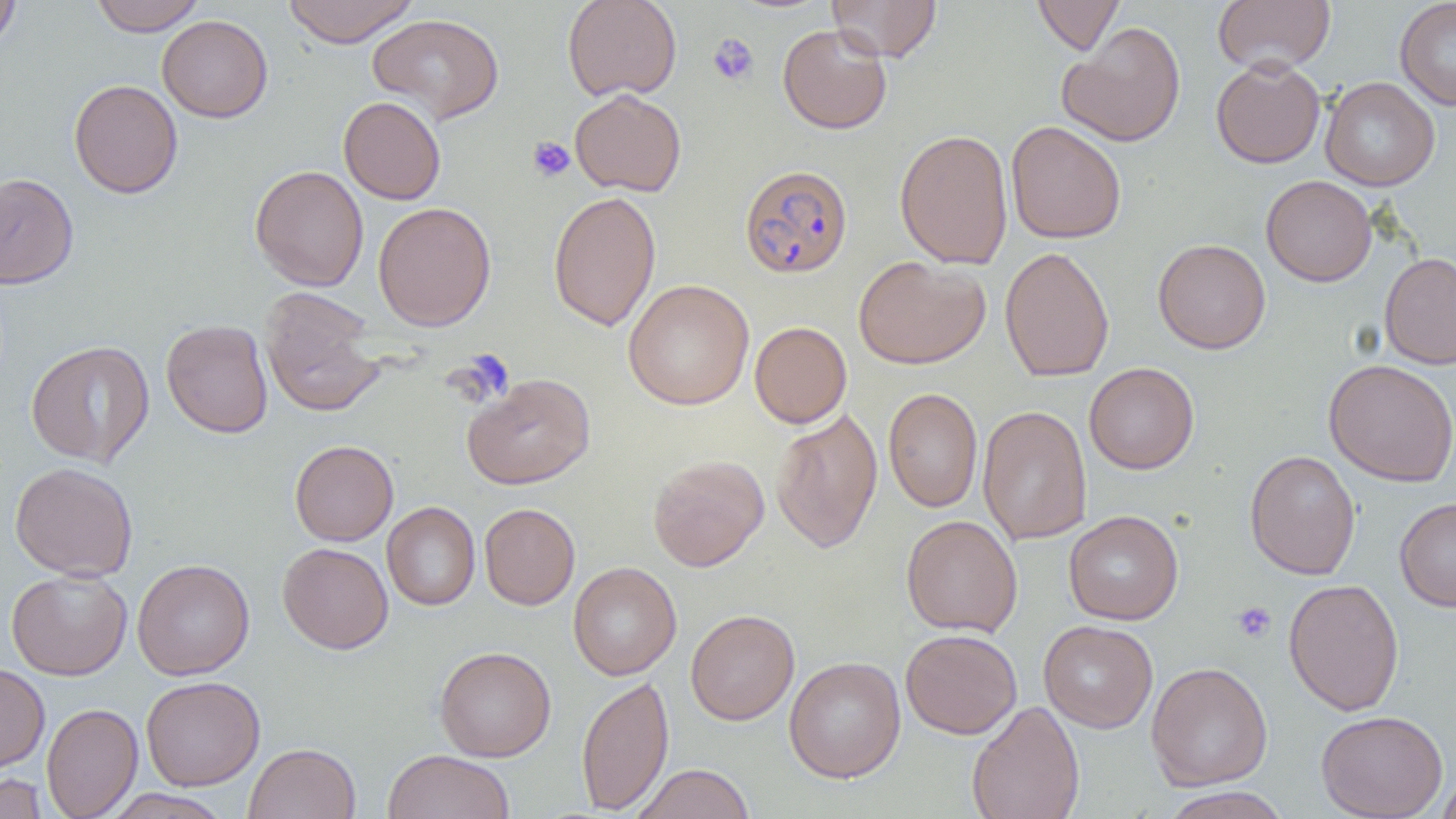
Summary:
  - Coordinate format: approximate bounding boxes as named x1/y1/x2/y2 corners in pixels
  - Platelet locations: (x1=707, y1=33, x2=759, y2=86), (x1=527, y1=136, x2=576, y2=182), (x1=450, y1=348, x2=514, y2=407), (x1=1232, y1=601, x2=1276, y2=643)
  - Plasmodium falciparum-infected red blood cell locations: (x1=739, y1=164, x2=853, y2=277)
  - Uninfected red blood cell locations: (x1=0, y1=0, x2=21, y2=54), (x1=90, y1=0, x2=206, y2=36), (x1=282, y1=0, x2=419, y2=47), (x1=562, y1=0, x2=682, y2=101), (x1=827, y1=0, x2=941, y2=62), (x1=1032, y1=0, x2=1124, y2=55), (x1=1213, y1=0, x2=1335, y2=75), (x1=1394, y1=0, x2=1456, y2=110), (x1=367, y1=13, x2=504, y2=124), (x1=157, y1=15, x2=273, y2=123), (x1=1057, y1=21, x2=1187, y2=147), (x1=777, y1=24, x2=892, y2=134), (x1=1210, y1=57, x2=1325, y2=168), (x1=1320, y1=76, x2=1440, y2=191), (x1=68, y1=78, x2=183, y2=198), (x1=570, y1=89, x2=686, y2=197), (x1=338, y1=96, x2=446, y2=205), (x1=1006, y1=121, x2=1126, y2=244), (x1=895, y1=128, x2=1013, y2=270), (x1=249, y1=164, x2=369, y2=291), (x1=0, y1=172, x2=79, y2=289), (x1=1261, y1=175, x2=1377, y2=287), (x1=548, y1=190, x2=661, y2=331), (x1=373, y1=201, x2=496, y2=332), (x1=1153, y1=238, x2=1271, y2=354), (x1=1000, y1=246, x2=1114, y2=382), (x1=1379, y1=253, x2=1456, y2=369), (x1=853, y1=255, x2=990, y2=369), (x1=623, y1=279, x2=754, y2=410), (x1=259, y1=287, x2=386, y2=418), (x1=161, y1=319, x2=273, y2=438), (x1=749, y1=321, x2=852, y2=428), (x1=25, y1=340, x2=155, y2=467), (x1=1324, y1=359, x2=1456, y2=487), (x1=1084, y1=362, x2=1199, y2=474), (x1=462, y1=373, x2=596, y2=489), (x1=883, y1=387, x2=983, y2=512), (x1=977, y1=405, x2=1092, y2=545), (x1=770, y1=407, x2=883, y2=554), (x1=290, y1=440, x2=398, y2=546), (x1=1244, y1=449, x2=1361, y2=580), (x1=648, y1=454, x2=769, y2=571), (x1=10, y1=461, x2=138, y2=581), (x1=1394, y1=497, x2=1456, y2=611), (x1=382, y1=502, x2=480, y2=610), (x1=479, y1=503, x2=580, y2=610), (x1=1063, y1=510, x2=1184, y2=625), (x1=901, y1=515, x2=1023, y2=637), (x1=277, y1=542, x2=393, y2=654), (x1=132, y1=558, x2=255, y2=680), (x1=568, y1=562, x2=682, y2=679), (x1=6, y1=569, x2=132, y2=680), (x1=1283, y1=578, x2=1404, y2=716), (x1=685, y1=609, x2=800, y2=725), (x1=1038, y1=620, x2=1158, y2=733), (x1=900, y1=628, x2=1022, y2=739), (x1=434, y1=646, x2=556, y2=761), (x1=783, y1=656, x2=906, y2=782), (x1=1146, y1=661, x2=1273, y2=790), (x1=0, y1=663, x2=50, y2=774), (x1=141, y1=675, x2=265, y2=790), (x1=576, y1=675, x2=674, y2=814), (x1=967, y1=700, x2=1086, y2=819), (x1=41, y1=702, x2=142, y2=818), (x1=1316, y1=710, x2=1448, y2=819), (x1=244, y1=742, x2=360, y2=819), (x1=383, y1=749, x2=515, y2=819), (x1=631, y1=763, x2=754, y2=819), (x1=1436, y1=767, x2=1456, y2=819), (x1=0, y1=773, x2=48, y2=819), (x1=1159, y1=786, x2=1291, y2=819), (x1=103, y1=789, x2=232, y2=819)
  - Slide-level diagnosis: Plasmodium falciparum
  - Field of view: one of a larger specimen
  - Preparation: thin blood smear
  - Image size: 1456×819 pixels
  - Modality: light microscopy
  - Magnification: 1000x